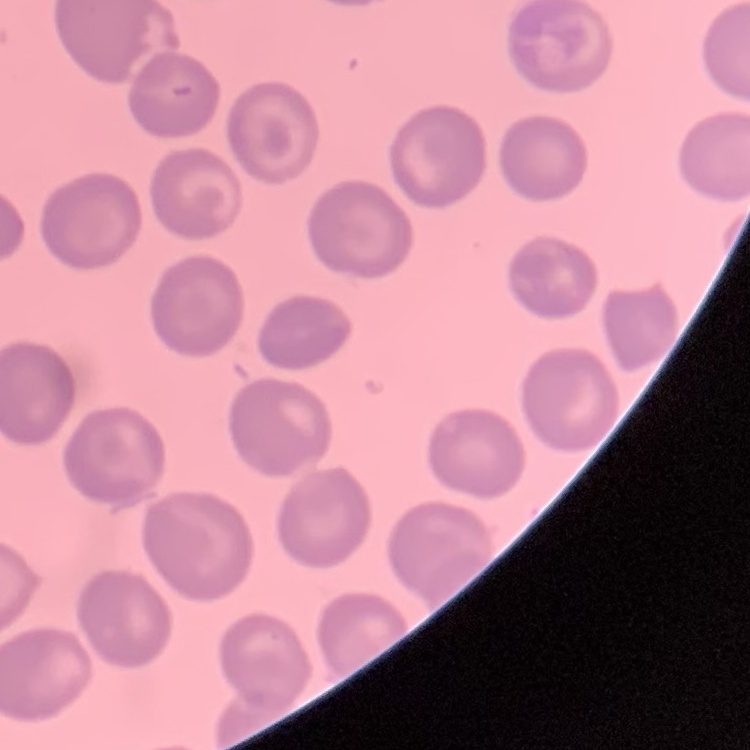
erythrocyte morphology = no rouleaux formation
stain = Field's or Giemsa
preparation = thin blood smear
image type = one tile cut from a larger photomicrograph